Report the malaria status of this cell.
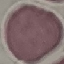
It is uninfected.

Photographed with a smartphone camera at the microscope eyepiece. Thin smear of blood. Cell patch, automatically extracted from a larger field of view and resized to 64 × 64 pixels. Giemsa-stained preparation.